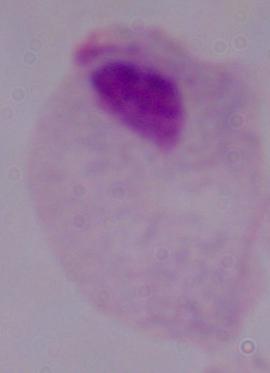

modality: photomicrograph
identification: trichomonad
magnification: 1000x